Give the extent of all Plasmodium vivax-infected red blood cells.
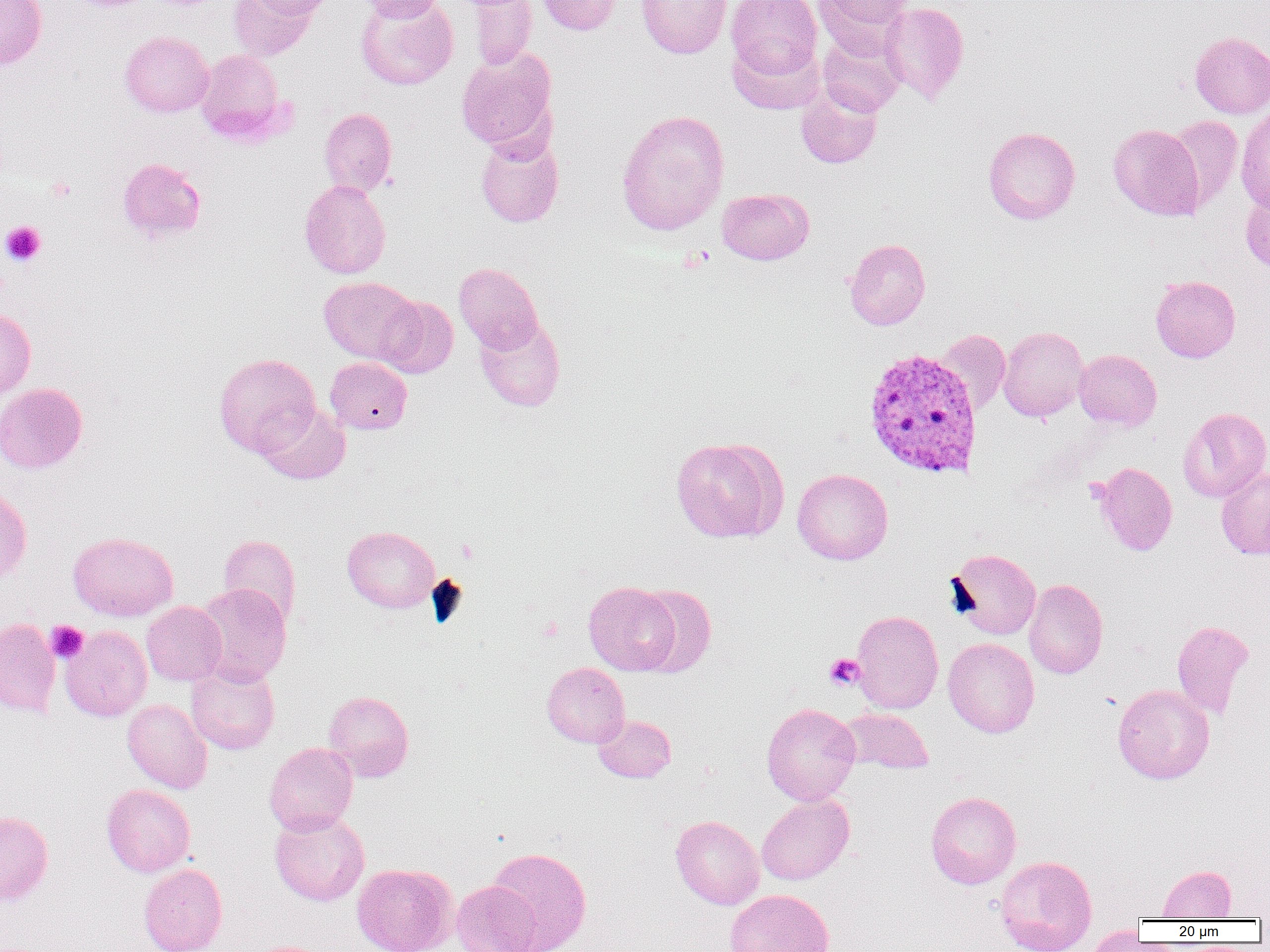

Approximate bounding boxes as (x1, y1, x2, y2) in pixels.
Plasmodium vivax-infected red blood cells: (862, 346, 983, 479).

slide-level diagnosis = Plasmodium vivax
magnification = 1000x
field of view = single
image size = 1270×952 pixels
modality = light microscopy
preparation = thin blood film
platelet locations = approximate bounding boxes as (x1, y1, x2, y2) in pixels: (47, 176, 77, 202), (1, 221, 46, 266), (455, 539, 478, 563), (46, 621, 88, 663), (824, 653, 865, 690)
uninfected red blood cell locations = approximate bounding boxes as (x1, y1, x2, y2) in pixels: (0, 0, 47, 70), (228, 0, 318, 60), (247, 0, 336, 20), (355, 0, 458, 90), (359, 0, 449, 21), (470, 0, 536, 70), (537, 0, 620, 35), (636, 0, 732, 59), (725, 0, 822, 80), (815, 0, 912, 50), (880, 2, 969, 104), (119, 31, 214, 117), (1190, 31, 1270, 118), (818, 34, 905, 116), (727, 38, 823, 115), (196, 48, 285, 143), (455, 48, 557, 153), (796, 84, 883, 169), (1235, 105, 1270, 211), (319, 107, 397, 196), (616, 109, 729, 236), (1165, 115, 1243, 210), (1108, 124, 1204, 221), (983, 126, 1080, 224), (475, 134, 564, 227), (117, 157, 207, 243), (299, 179, 391, 279), (1241, 185, 1270, 273), (717, 188, 814, 265), (844, 238, 931, 330), (454, 263, 543, 354), (1150, 275, 1241, 363), (319, 276, 420, 365), (378, 295, 458, 378), (0, 309, 36, 399), (475, 315, 566, 412), (997, 326, 1088, 421), (935, 329, 1011, 414), (1074, 349, 1162, 431), (214, 353, 320, 457), (325, 357, 412, 434), (0, 383, 87, 473), (257, 402, 350, 485), (1178, 407, 1270, 502), (670, 436, 787, 543), (1094, 462, 1177, 556), (1216, 467, 1270, 559), (792, 468, 893, 565), (0, 485, 32, 582), (342, 526, 440, 613), (68, 531, 178, 621), (218, 534, 302, 627), (947, 548, 1041, 640), (1024, 578, 1108, 679), (584, 581, 679, 675), (195, 582, 292, 685), (633, 584, 716, 678), (141, 601, 226, 686), (851, 609, 944, 714), (0, 618, 60, 716), (1172, 620, 1254, 719), (60, 626, 152, 721), (943, 637, 1040, 738), (185, 660, 280, 755), (542, 662, 630, 747), (1112, 683, 1214, 784), (324, 690, 414, 781), (122, 698, 212, 793), (761, 703, 861, 805), (841, 708, 935, 775), (593, 715, 676, 783), (264, 742, 358, 835), (101, 784, 195, 877), (925, 791, 1021, 889), (756, 794, 854, 885), (0, 810, 53, 905), (269, 810, 370, 906), (670, 815, 764, 909), (486, 846, 592, 952), (995, 854, 1097, 952), (352, 862, 457, 952), (138, 863, 227, 952), (1156, 864, 1237, 920), (451, 880, 541, 952), (724, 889, 834, 952), (1083, 924, 1147, 951)